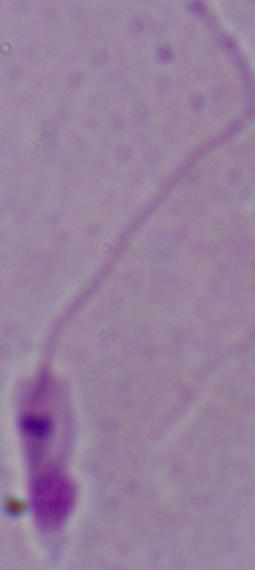 A Leishmania parasite is seen. Micrograph. 1000x magnification.